Give the position of every leukocyte visible.
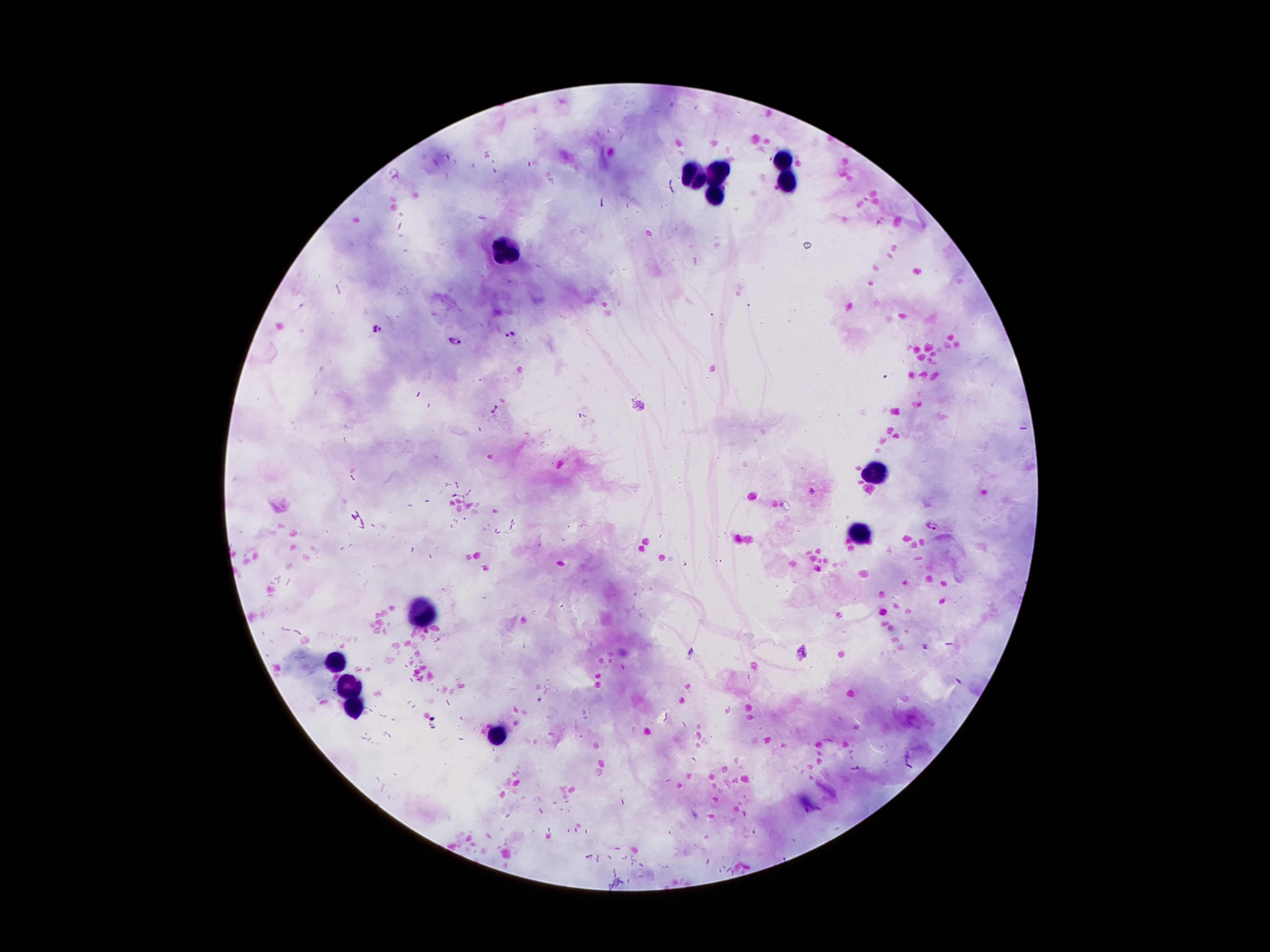

Approximate centers as [x, y] in pixels.
Leukocytes: [784, 155], [720, 172], [695, 178], [784, 183], [715, 195], [506, 251], [878, 475], [863, 532], [422, 615], [336, 661], [349, 686], [356, 709], [498, 735].

Summary:
  - Malaria parasite locations: [378, 330], [511, 334], [455, 340], [931, 524]
  - Field of view: single
  - Capture: smartphone camera through the microscope eyepiece
  - Stain: Giemsa
  - Image size: 1270×952 pixels
  - Patient malaria status: positive for Plasmodium falciparum
  - Preparation: thick blood smear
  - Magnification: 100x